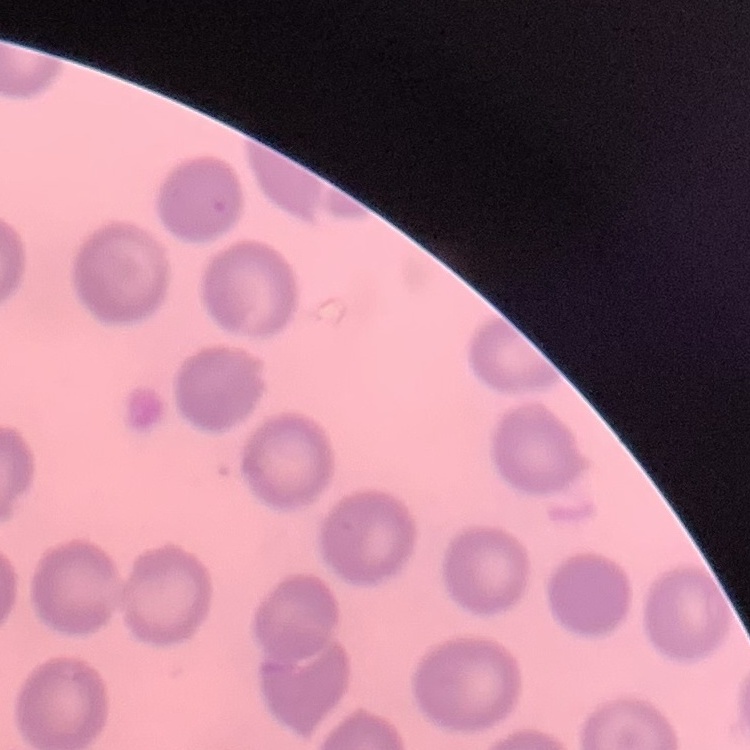
red blood cell morphology = no rouleaux formation
stain = Field's or Giemsa
preparation = thin blood smear
image type = square crop of a larger photomicrograph